Locate and identify every blood parasite.
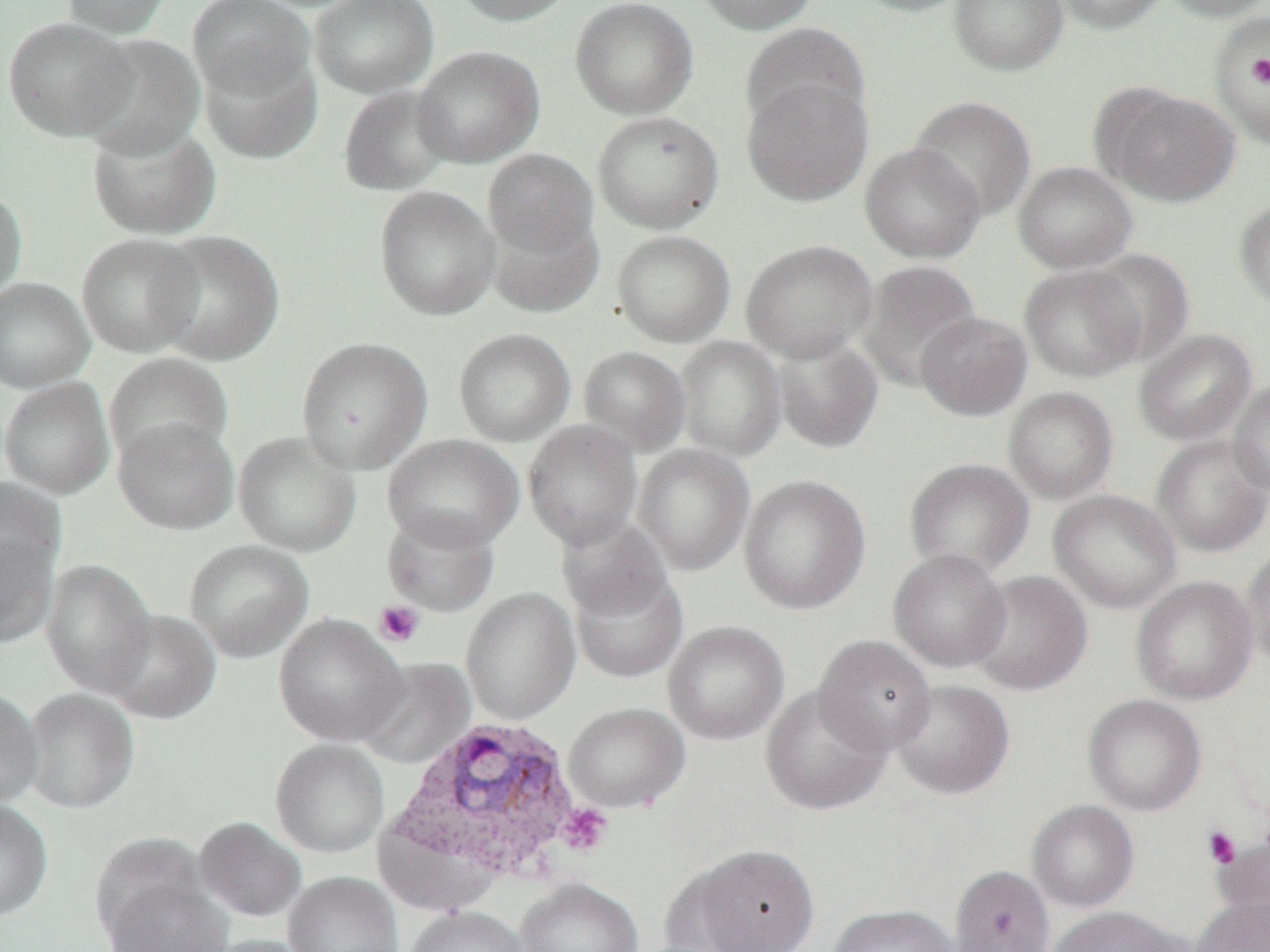
Approximate bounding boxes as (x1,y1)-(x2,y2) corner pairs in pixels.
Plasmodium vivax-infected red blood cells: (390,716)-(584,880).
No Plasmodium falciparum, Plasmodium ovale, Plasmodium malariae, Babesia divergens, or Trypanosoma brucei observed.

{
  "slide_level_diagnosis": "Plasmodium vivax",
  "magnification": "1000x",
  "image_size": "1270×952 pixels",
  "field_of_view": "one of a larger specimen",
  "platelet_locations": "approximate bounding boxes as (x1,y1)-(x2,y2) corner pairs in pixels: (1247,55)-(1270,88), (373,600)-(425,647), (556,802)-(613,856), (1202,825)-(1242,869)",
  "uninfected_red_blood_cell_locations": "approximate bounding boxes as (x1,y1)-(x2,y2) corner pairs in pixels: (58,0)-(175,38), (188,0)-(315,102), (310,0)-(438,98), (450,0)-(578,26), (570,0)-(698,120), (695,0)-(819,35), (847,0)-(976,17), (948,0)-(1069,76), (1052,0)-(1170,35), (1158,0)-(1270,21), (1208,11)-(1270,150), (3,17)-(136,141), (740,23)-(871,136), (79,33)-(206,157), (411,44)-(545,168), (199,48)-(323,163), (741,75)-(874,205), (1096,83)-(1241,206), (338,85)-(456,195), (908,95)-(1037,222), (592,110)-(724,234), (87,120)-(222,239), (859,142)-(986,264), (483,148)-(599,258), (1013,161)-(1137,274), (0,185)-(27,304), (374,186)-(500,320), (1233,199)-(1270,311), (485,208)-(604,317), (150,230)-(285,366), (612,230)-(735,347), (76,233)-(204,357), (741,239)-(878,363), (1083,248)-(1196,366), (857,259)-(982,392), (1019,264)-(1146,382), (0,277)-(94,393), (916,311)-(1033,421), (453,327)-(575,446), (1134,328)-(1256,446), (771,332)-(884,453), (296,336)-(433,474), (675,336)-(787,461), (578,345)-(691,455), (104,352)-(234,467), (0,377)-(115,498), (1228,379)-(1270,496), (1003,386)-(1119,504), (113,416)-(239,534), (523,421)-(643,551), (234,430)-(362,557), (382,434)-(524,553), (1151,434)-(1270,557), (633,444)-(755,576), (904,457)-(1035,579), (739,473)-(870,615), (1049,489)-(1181,613), (382,508)-(501,616), (556,515)-(674,628), (0,528)-(60,647), (184,539)-(314,662), (1240,545)-(1270,669), (888,548)-(1012,672), (40,559)-(157,696), (567,559)-(688,684), (969,570)-(1092,696), (1130,576)-(1258,705), (461,587)-(581,724), (102,609)-(222,724), (273,613)-(408,746), (663,620)-(790,745), (813,634)-(937,756), (354,656)-(477,769), (889,679)-(1015,800), (760,685)-(892,816), (0,687)-(43,809), (22,687)-(140,814), (1082,693)-(1207,816), (563,702)-(690,813), (270,738)-(390,858), (0,799)-(53,923), (1028,800)-(1139,912), (194,816)-(306,922), (1212,828)-(1270,931), (681,844)-(820,952), (949,865)-(1056,952), (283,871)-(403,952), (102,875)-(234,952), (515,878)-(644,952), (1191,896)-(1270,952), (827,904)-(961,952), (404,905)-(531,952), (1046,906)-(1186,952), (204,935)-(316,952)",
  "modality": "light microscopy",
  "preparation": "thin blood smear"
}